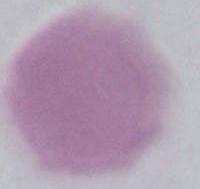

{
  "magnification": "1000x",
  "identification": "erythrocyte",
  "modality": "micrograph"
}